Point out each malaria parasite.
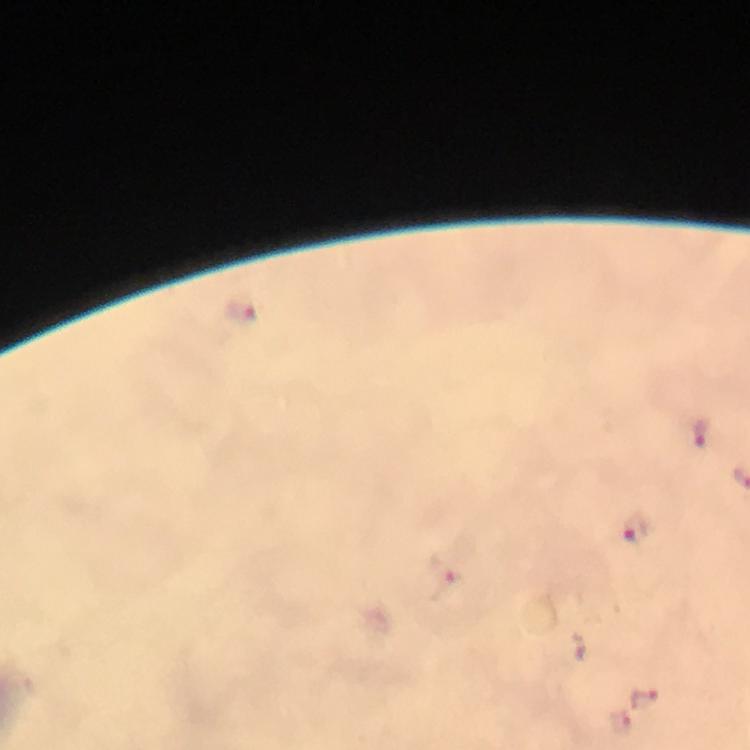

Approximate object centers, in pixels from the top-left corner.
Malaria parasites: (x=243, y=311), (x=700, y=433), (x=634, y=528), (x=443, y=579), (x=644, y=699), (x=617, y=723).

Immersion oil was used. From a malaria diagnostic workup. 100x magnification. Thick blood smear. Cropped region of a single field of view. Giemsa-stained preparation. Smartphone photograph taken through a microscope. Image is 750×750 pixels.